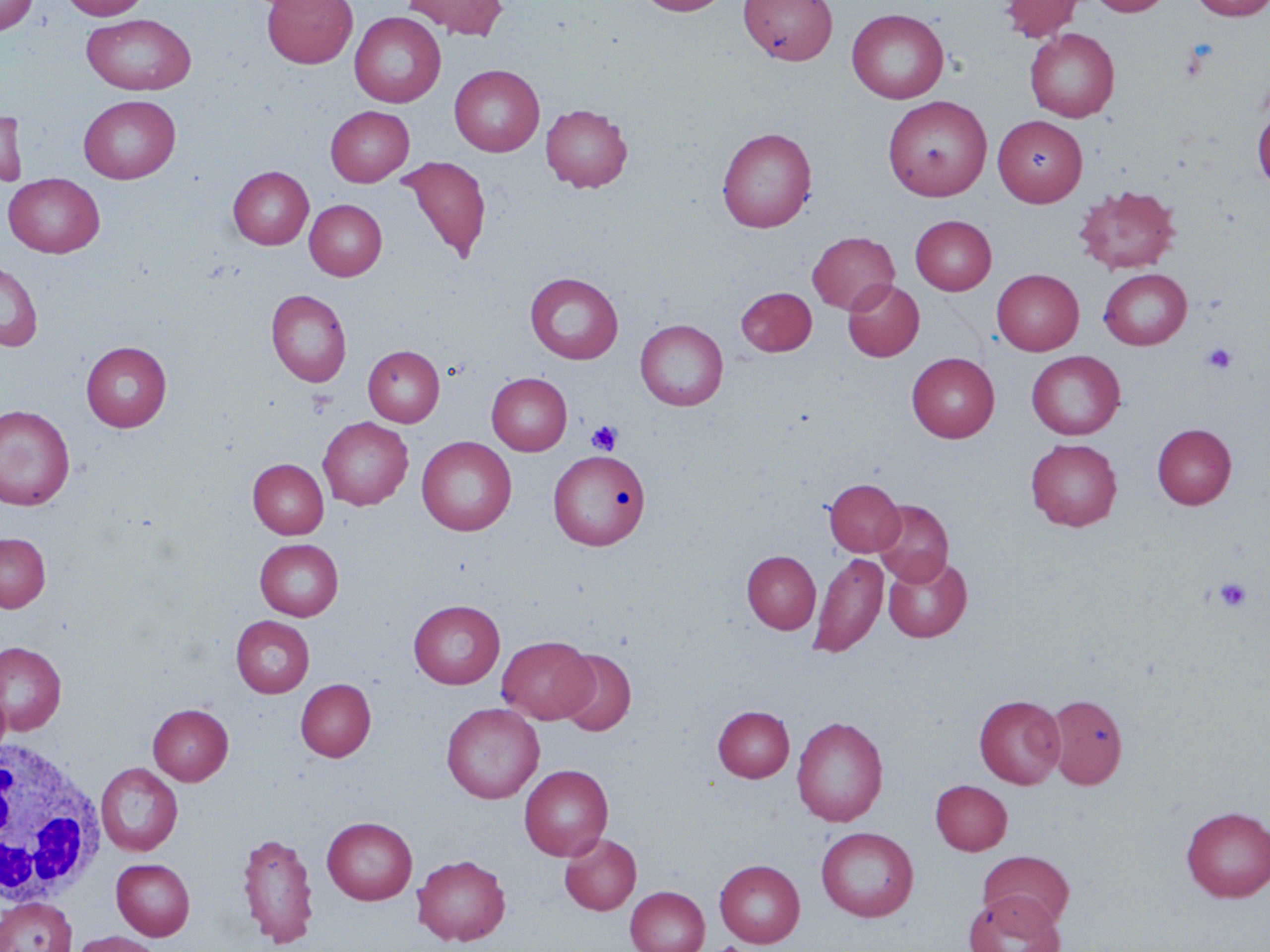
slide_level_diagnosis: no evidence of blood parasites
white_blood_cell_locations: 'approximate bounding boxes as named x1/y1/x2/y2 corners in pixels: (x1=0, y1=736, x2=104, y2=910)'
image_size: 1270×952 pixels
preparation: thin blood smear
uninfected_red_blood_cell_locations: 'approximate bounding boxes as named x1/y1/x2/y2 corners in pixels: (x1=0, y1=0, x2=38, y2=34), (x1=61, y1=0, x2=150, y2=20), (x1=262, y1=0, x2=357, y2=68), (x1=403, y1=0, x2=509, y2=38), (x1=636, y1=0, x2=730, y2=16), (x1=740, y1=0, x2=837, y2=65), (x1=1000, y1=0, x2=1083, y2=41), (x1=1088, y1=0, x2=1173, y2=16), (x1=1189, y1=0, x2=1270, y2=19), (x1=847, y1=8, x2=949, y2=103), (x1=349, y1=11, x2=446, y2=107), (x1=82, y1=14, x2=197, y2=95), (x1=1025, y1=28, x2=1120, y2=122), (x1=450, y1=64, x2=544, y2=156), (x1=79, y1=94, x2=181, y2=183), (x1=882, y1=95, x2=992, y2=201), (x1=541, y1=103, x2=633, y2=192), (x1=325, y1=105, x2=414, y2=186), (x1=1252, y1=105, x2=1270, y2=191), (x1=0, y1=110, x2=29, y2=187), (x1=993, y1=115, x2=1087, y2=206), (x1=717, y1=127, x2=816, y2=232), (x1=397, y1=156, x2=491, y2=264), (x1=228, y1=166, x2=313, y2=249), (x1=4, y1=173, x2=105, y2=258), (x1=1074, y1=184, x2=1181, y2=274), (x1=305, y1=199, x2=387, y2=280), (x1=910, y1=215, x2=996, y2=295), (x1=807, y1=231, x2=899, y2=314), (x1=0, y1=259, x2=43, y2=352), (x1=1099, y1=268, x2=1192, y2=349), (x1=992, y1=269, x2=1084, y2=355), (x1=525, y1=272, x2=623, y2=364), (x1=842, y1=279, x2=924, y2=361), (x1=736, y1=287, x2=817, y2=356), (x1=266, y1=289, x2=351, y2=387), (x1=635, y1=319, x2=728, y2=410), (x1=81, y1=341, x2=172, y2=431), (x1=363, y1=345, x2=445, y2=427), (x1=1027, y1=351, x2=1125, y2=439), (x1=907, y1=352, x2=999, y2=442), (x1=487, y1=372, x2=572, y2=455), (x1=0, y1=405, x2=75, y2=510), (x1=318, y1=417, x2=413, y2=509), (x1=1151, y1=423, x2=1237, y2=509), (x1=417, y1=436, x2=516, y2=536), (x1=1026, y1=438, x2=1122, y2=530), (x1=549, y1=450, x2=651, y2=549), (x1=248, y1=459, x2=329, y2=538), (x1=824, y1=478, x2=905, y2=556), (x1=873, y1=499, x2=953, y2=585), (x1=0, y1=532, x2=50, y2=612), (x1=255, y1=539, x2=343, y2=620), (x1=742, y1=550, x2=821, y2=634), (x1=809, y1=552, x2=888, y2=657), (x1=883, y1=555, x2=972, y2=642), (x1=409, y1=599, x2=505, y2=689), (x1=231, y1=615, x2=315, y2=697), (x1=498, y1=636, x2=596, y2=723), (x1=1, y1=641, x2=66, y2=735), (x1=556, y1=649, x2=636, y2=735), (x1=296, y1=679, x2=376, y2=761), (x1=0, y1=684, x2=11, y2=761), (x1=1046, y1=693, x2=1128, y2=788), (x1=975, y1=695, x2=1065, y2=788), (x1=441, y1=702, x2=544, y2=803), (x1=148, y1=704, x2=233, y2=784), (x1=713, y1=706, x2=794, y2=782), (x1=791, y1=716, x2=888, y2=827), (x1=96, y1=763, x2=183, y2=856), (x1=519, y1=764, x2=613, y2=860), (x1=931, y1=779, x2=1012, y2=855), (x1=1181, y1=806, x2=1270, y2=902), (x1=322, y1=816, x2=417, y2=904), (x1=816, y1=826, x2=918, y2=921), (x1=236, y1=831, x2=319, y2=948), (x1=560, y1=833, x2=641, y2=915), (x1=978, y1=850, x2=1075, y2=930), (x1=412, y1=854, x2=510, y2=945), (x1=111, y1=858, x2=195, y2=940), (x1=714, y1=859, x2=805, y2=946), (x1=625, y1=886, x2=710, y2=952), (x1=965, y1=892, x2=1063, y2=952), (x1=0, y1=898, x2=76, y2=952), (x1=70, y1=931, x2=164, y2=952)'
modality: optical microscopy
platelet_locations: 'approximate bounding boxes as named x1/y1/x2/y2 corners in pixels: (x1=1178, y1=42, x2=1215, y2=82), (x1=1201, y1=343, x2=1237, y2=375), (x1=586, y1=420, x2=622, y2=455), (x1=1214, y1=576, x2=1252, y2=613), (x1=709, y1=942, x2=755, y2=952)'
field_of_view: one of a larger specimen
stain: May-Grünwald-Giemsa
magnification: 1000x